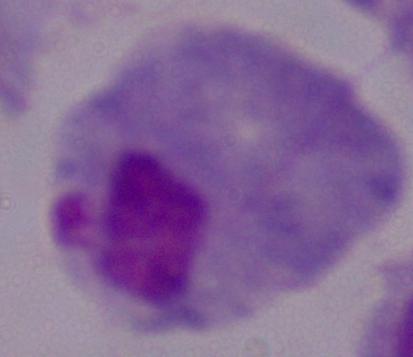

A trichomonad is shown. 1000x magnification. Photomicrograph.